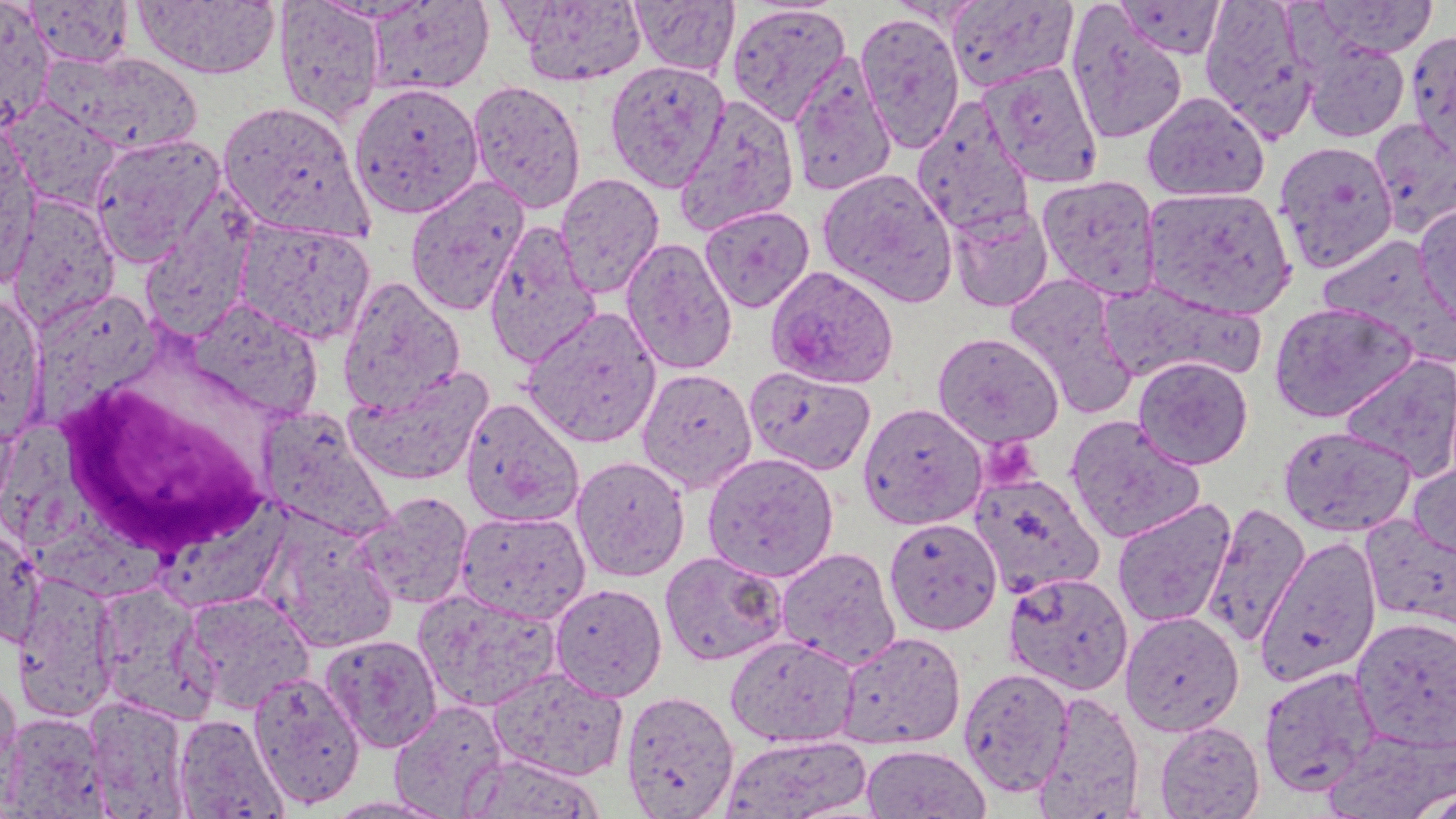

Summary:
  - Coordinate format: approximate bounding boxes as named x1/y1/x2/y2 corners in pixels
  - White blood cell locations: (x1=56, y1=381, x2=269, y2=560)
  - Uninfected red blood cell locations: (x1=134, y1=0, x2=281, y2=80), (x1=274, y1=0, x2=385, y2=125), (x1=510, y1=0, x2=649, y2=86), (x1=630, y1=0, x2=740, y2=77), (x1=945, y1=0, x2=1079, y2=93), (x1=1115, y1=0, x2=1227, y2=59), (x1=1308, y1=0, x2=1438, y2=59), (x1=0, y1=1, x2=55, y2=132), (x1=25, y1=1, x2=135, y2=67), (x1=365, y1=1, x2=494, y2=97), (x1=1199, y1=1, x2=1319, y2=142), (x1=726, y1=3, x2=852, y2=126), (x1=1065, y1=5, x2=1189, y2=146), (x1=855, y1=11, x2=965, y2=155), (x1=1406, y1=30, x2=1456, y2=163), (x1=1302, y1=40, x2=1411, y2=143), (x1=47, y1=50, x2=203, y2=156), (x1=787, y1=53, x2=898, y2=198), (x1=604, y1=59, x2=731, y2=192), (x1=982, y1=62, x2=1103, y2=187), (x1=467, y1=79, x2=587, y2=214), (x1=348, y1=81, x2=485, y2=219), (x1=1141, y1=91, x2=1270, y2=202), (x1=673, y1=94, x2=801, y2=237), (x1=3, y1=99, x2=124, y2=213), (x1=217, y1=100, x2=373, y2=241), (x1=911, y1=100, x2=1034, y2=238), (x1=1368, y1=117, x2=1456, y2=238), (x1=0, y1=128, x2=41, y2=291), (x1=89, y1=132, x2=227, y2=267), (x1=1274, y1=140, x2=1399, y2=273), (x1=816, y1=167, x2=958, y2=307), (x1=555, y1=172, x2=665, y2=299), (x1=1037, y1=174, x2=1162, y2=301), (x1=404, y1=176, x2=530, y2=317), (x1=1142, y1=186, x2=1297, y2=319), (x1=6, y1=194, x2=121, y2=333), (x1=947, y1=202, x2=1055, y2=313), (x1=1414, y1=202, x2=1456, y2=326), (x1=699, y1=205, x2=815, y2=313), (x1=233, y1=216, x2=376, y2=345), (x1=483, y1=220, x2=601, y2=369), (x1=621, y1=237, x2=737, y2=375), (x1=1003, y1=274, x2=1138, y2=417), (x1=337, y1=276, x2=466, y2=414), (x1=1099, y1=280, x2=1264, y2=386), (x1=0, y1=294, x2=47, y2=444), (x1=188, y1=298, x2=323, y2=422), (x1=1268, y1=301, x2=1418, y2=423), (x1=521, y1=306, x2=662, y2=449), (x1=932, y1=332, x2=1065, y2=449), (x1=1339, y1=353, x2=1456, y2=481), (x1=1133, y1=355, x2=1254, y2=470), (x1=344, y1=364, x2=494, y2=486), (x1=744, y1=365, x2=877, y2=476), (x1=636, y1=367, x2=758, y2=494), (x1=460, y1=398, x2=584, y2=527), (x1=857, y1=402, x2=988, y2=530), (x1=256, y1=408, x2=396, y2=542), (x1=1065, y1=415, x2=1206, y2=543), (x1=1279, y1=425, x2=1415, y2=537), (x1=701, y1=451, x2=840, y2=583), (x1=570, y1=455, x2=690, y2=582), (x1=1408, y1=458, x2=1456, y2=565), (x1=968, y1=471, x2=1104, y2=598), (x1=354, y1=490, x2=474, y2=610), (x1=1111, y1=498, x2=1236, y2=629), (x1=1201, y1=502, x2=1311, y2=646), (x1=456, y1=509, x2=591, y2=624), (x1=1361, y1=516, x2=1456, y2=632), (x1=883, y1=517, x2=1003, y2=636), (x1=0, y1=524, x2=44, y2=650), (x1=267, y1=525, x2=398, y2=654), (x1=1255, y1=536, x2=1382, y2=686), (x1=776, y1=546, x2=901, y2=670), (x1=659, y1=550, x2=789, y2=667), (x1=12, y1=571, x2=122, y2=722), (x1=1003, y1=571, x2=1134, y2=695), (x1=92, y1=581, x2=219, y2=725), (x1=549, y1=583, x2=668, y2=701), (x1=415, y1=589, x2=562, y2=712), (x1=180, y1=591, x2=315, y2=714), (x1=1120, y1=611, x2=1244, y2=736), (x1=1351, y1=615, x2=1456, y2=748), (x1=836, y1=631, x2=966, y2=750), (x1=320, y1=634, x2=443, y2=753), (x1=725, y1=634, x2=859, y2=747), (x1=1258, y1=665, x2=1382, y2=799), (x1=958, y1=666, x2=1075, y2=797), (x1=489, y1=667, x2=629, y2=781), (x1=247, y1=671, x2=366, y2=809), (x1=0, y1=677, x2=22, y2=792), (x1=620, y1=690, x2=740, y2=818), (x1=1033, y1=691, x2=1145, y2=819), (x1=85, y1=697, x2=190, y2=816), (x1=389, y1=699, x2=510, y2=817), (x1=1, y1=712, x2=110, y2=818), (x1=172, y1=713, x2=289, y2=819), (x1=1155, y1=720, x2=1265, y2=818), (x1=718, y1=733, x2=873, y2=819), (x1=860, y1=744, x2=992, y2=818), (x1=460, y1=753, x2=605, y2=817), (x1=1415, y1=786, x2=1456, y2=819)
  - Plasmodium ovale-infected red blood cell locations: (x1=765, y1=265, x2=900, y2=389)
  - Platelet locations: (x1=983, y1=435, x2=1038, y2=485)
  - Slide-level diagnosis: Plasmodium ovale
  - Field of view: single
  - Modality: light microscopy
  - Magnification: 1000x
  - Stain: May-Grünwald-Giemsa
  - Preparation: thin blood film
  - Image size: 1456×819 pixels